Outline each blood parasite and name the species.
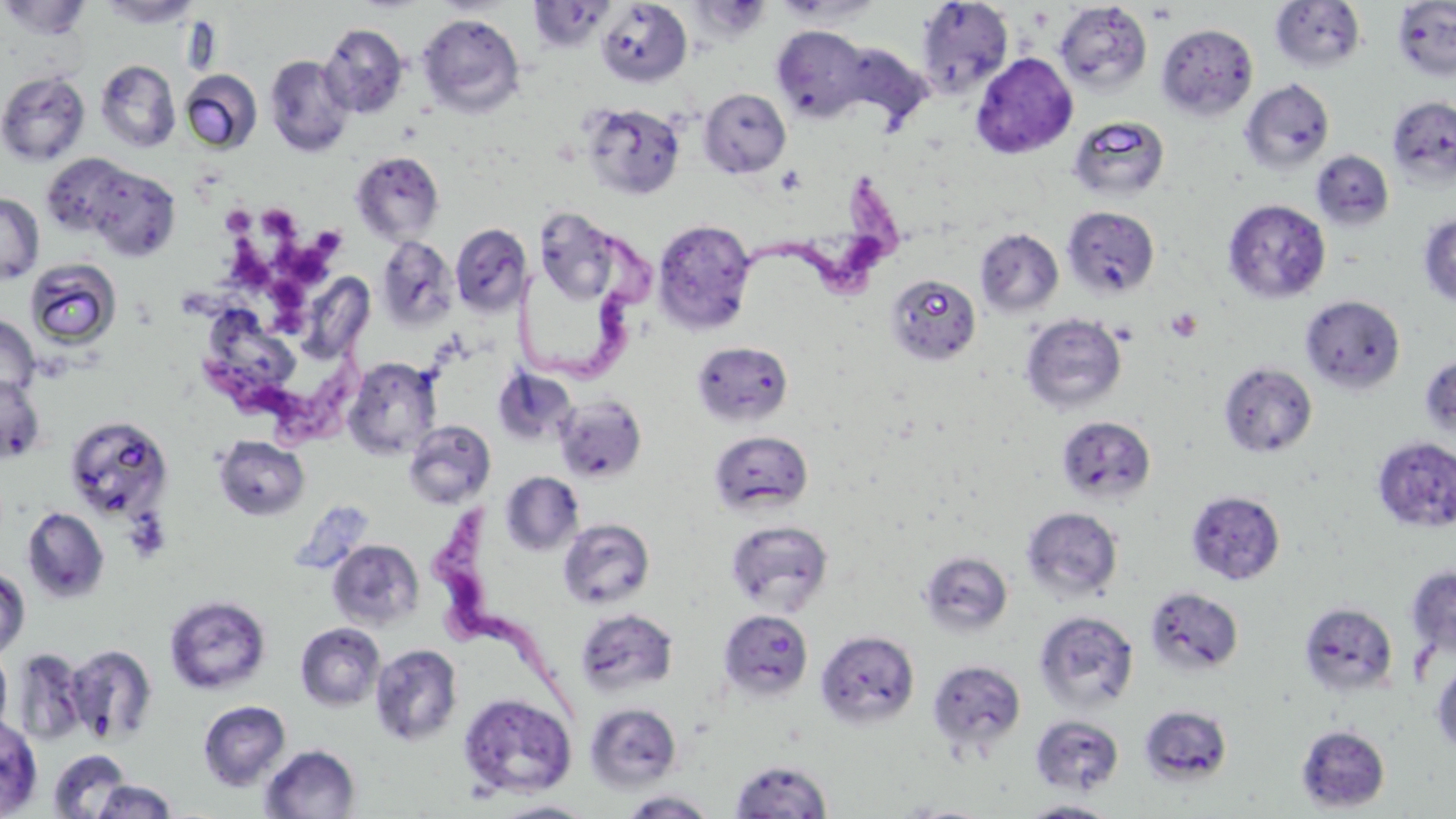
Approximate bounding boxes as named x1/y1/x2/y2 corners in pixels.
Trypanosoma brucei: (x1=740, y1=172, x2=906, y2=298), (x1=515, y1=226, x2=670, y2=384), (x1=205, y1=344, x2=395, y2=452), (x1=421, y1=510, x2=582, y2=718).
No Plasmodium falciparum, Plasmodium ovale, Plasmodium malariae, Plasmodium vivax, or Babesia divergens observed.

slide-level diagnosis = Trypanosoma brucei
preparation = thin blood smear
uninfected red blood cell locations = approximate bounding boxes as named x1/y1/x2/y2 corners in pixels: (x1=1, y1=0, x2=91, y2=40), (x1=98, y1=0, x2=202, y2=28), (x1=772, y1=0, x2=884, y2=25), (x1=527, y1=1, x2=615, y2=53), (x1=596, y1=1, x2=692, y2=87), (x1=915, y1=1, x2=1013, y2=100), (x1=1270, y1=1, x2=1366, y2=73), (x1=1391, y1=1, x2=1456, y2=81), (x1=1054, y1=2, x2=1152, y2=95), (x1=418, y1=13, x2=526, y2=117), (x1=1156, y1=23, x2=1258, y2=121), (x1=319, y1=24, x2=409, y2=118), (x1=771, y1=25, x2=871, y2=122), (x1=970, y1=52, x2=1078, y2=159), (x1=264, y1=54, x2=355, y2=157), (x1=95, y1=59, x2=181, y2=153), (x1=0, y1=70, x2=91, y2=166), (x1=180, y1=70, x2=262, y2=153), (x1=1239, y1=78, x2=1336, y2=175), (x1=698, y1=88, x2=791, y2=178), (x1=1387, y1=96, x2=1456, y2=189), (x1=581, y1=102, x2=685, y2=201), (x1=1067, y1=116, x2=1170, y2=201), (x1=351, y1=150, x2=445, y2=244), (x1=1311, y1=150, x2=1395, y2=231), (x1=80, y1=163, x2=182, y2=261), (x1=0, y1=192, x2=43, y2=285), (x1=1223, y1=199, x2=1332, y2=305), (x1=1061, y1=206, x2=1160, y2=298), (x1=533, y1=208, x2=625, y2=306), (x1=1418, y1=212, x2=1456, y2=306), (x1=652, y1=219, x2=757, y2=336), (x1=450, y1=223, x2=532, y2=317), (x1=975, y1=228, x2=1064, y2=318), (x1=376, y1=235, x2=459, y2=330), (x1=25, y1=258, x2=122, y2=350), (x1=886, y1=274, x2=982, y2=366), (x1=308, y1=282, x2=374, y2=355), (x1=1300, y1=294, x2=1406, y2=395), (x1=202, y1=304, x2=292, y2=380), (x1=1020, y1=313, x2=1128, y2=415), (x1=0, y1=314, x2=40, y2=400), (x1=692, y1=341, x2=794, y2=427), (x1=1420, y1=355, x2=1456, y2=440), (x1=342, y1=356, x2=441, y2=459), (x1=1218, y1=361, x2=1318, y2=459), (x1=494, y1=368, x2=577, y2=447), (x1=0, y1=374, x2=45, y2=464), (x1=553, y1=394, x2=648, y2=484), (x1=64, y1=416, x2=173, y2=523), (x1=1056, y1=416, x2=1156, y2=505), (x1=403, y1=419, x2=495, y2=509), (x1=709, y1=430, x2=814, y2=517), (x1=213, y1=434, x2=310, y2=521), (x1=1372, y1=435, x2=1456, y2=534), (x1=500, y1=472, x2=584, y2=555), (x1=22, y1=506, x2=110, y2=604), (x1=1021, y1=507, x2=1124, y2=603), (x1=558, y1=517, x2=655, y2=610), (x1=724, y1=519, x2=834, y2=615), (x1=327, y1=539, x2=425, y2=631), (x1=919, y1=551, x2=1014, y2=638), (x1=1405, y1=564, x2=1456, y2=663), (x1=0, y1=565, x2=30, y2=660), (x1=1144, y1=585, x2=1244, y2=677), (x1=164, y1=595, x2=272, y2=694), (x1=1299, y1=602, x2=1399, y2=698), (x1=575, y1=607, x2=679, y2=698), (x1=718, y1=609, x2=814, y2=702), (x1=1033, y1=609, x2=1140, y2=713), (x1=295, y1=622, x2=385, y2=711), (x1=815, y1=629, x2=921, y2=730), (x1=370, y1=643, x2=463, y2=747), (x1=66, y1=644, x2=158, y2=744), (x1=0, y1=645, x2=12, y2=739), (x1=11, y1=648, x2=87, y2=746), (x1=1431, y1=656, x2=1456, y2=758), (x1=926, y1=658, x2=1027, y2=759), (x1=458, y1=692, x2=577, y2=798), (x1=198, y1=700, x2=291, y2=791), (x1=584, y1=701, x2=682, y2=793), (x1=1138, y1=704, x2=1234, y2=786), (x1=0, y1=715, x2=42, y2=816), (x1=1029, y1=715, x2=1126, y2=795), (x1=1295, y1=724, x2=1390, y2=813), (x1=259, y1=744, x2=361, y2=819), (x1=48, y1=749, x2=133, y2=819), (x1=729, y1=759, x2=834, y2=818), (x1=91, y1=780, x2=178, y2=818), (x1=617, y1=789, x2=719, y2=818), (x1=1015, y1=799, x2=1124, y2=817), (x1=492, y1=800, x2=599, y2=818), (x1=887, y1=801, x2=999, y2=818)
modality = light microscopy
platelet locations = approximate bounding boxes as named x1/y1/x2/y2 corners in pixels: (x1=1147, y1=3, x2=1178, y2=25), (x1=774, y1=164, x2=806, y2=196), (x1=220, y1=206, x2=257, y2=236), (x1=267, y1=207, x2=302, y2=246), (x1=316, y1=227, x2=347, y2=254), (x1=227, y1=238, x2=280, y2=293), (x1=273, y1=242, x2=340, y2=288), (x1=275, y1=282, x2=312, y2=318), (x1=1165, y1=307, x2=1203, y2=343), (x1=272, y1=310, x2=311, y2=340)
stain = May-Grünwald-Giemsa
image size = 1456×819 pixels
field of view = one of a larger specimen
magnification = 1000x